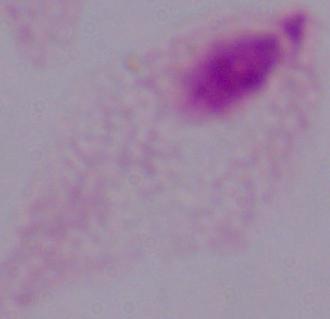
A trichomonad is seen. 1000x magnification. Photomicrograph.